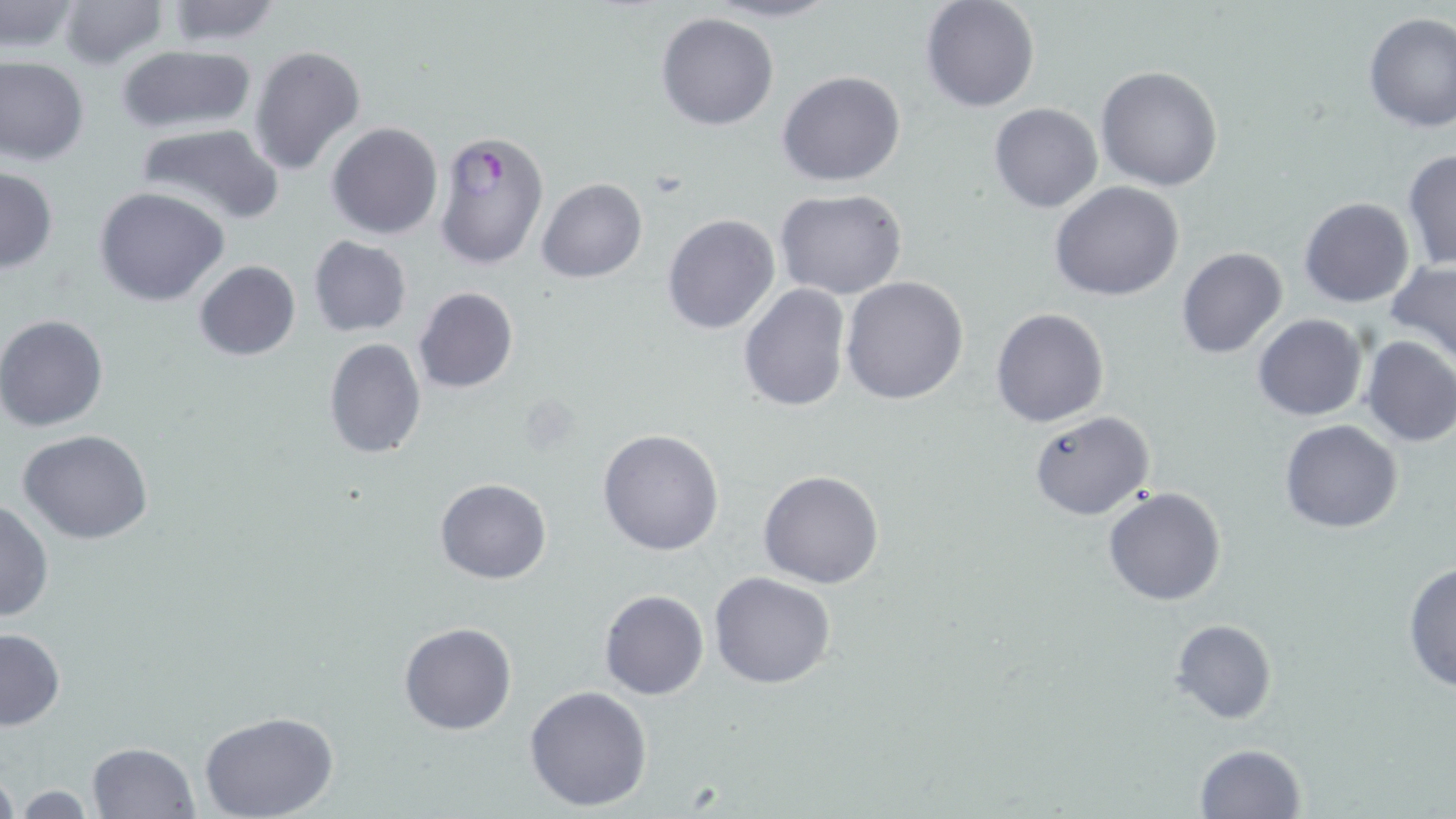
Summary:
  - Coordinate format: approximate bounding boxes as named x1/y1/x2/y2 corners in pixels
  - Uninfected red blood cell locations: (x1=58, y1=0, x2=167, y2=69), (x1=701, y1=0, x2=841, y2=24), (x1=919, y1=1, x2=1040, y2=113), (x1=1, y1=2, x2=80, y2=53), (x1=163, y1=2, x2=286, y2=48), (x1=655, y1=10, x2=780, y2=131), (x1=1361, y1=11, x2=1456, y2=131), (x1=114, y1=43, x2=260, y2=136), (x1=249, y1=44, x2=366, y2=178), (x1=0, y1=56, x2=89, y2=166), (x1=1095, y1=66, x2=1224, y2=191), (x1=777, y1=69, x2=907, y2=187), (x1=989, y1=103, x2=1104, y2=214), (x1=133, y1=122, x2=285, y2=227), (x1=327, y1=122, x2=444, y2=239), (x1=1401, y1=149, x2=1455, y2=272), (x1=0, y1=166, x2=58, y2=273), (x1=537, y1=178, x2=647, y2=283), (x1=1049, y1=181, x2=1184, y2=302), (x1=94, y1=186, x2=230, y2=306), (x1=774, y1=188, x2=908, y2=299), (x1=1299, y1=196, x2=1417, y2=308), (x1=661, y1=213, x2=780, y2=334), (x1=308, y1=236, x2=412, y2=336), (x1=1176, y1=248, x2=1288, y2=361), (x1=1386, y1=259, x2=1456, y2=366), (x1=193, y1=260, x2=301, y2=361), (x1=841, y1=277, x2=969, y2=405), (x1=738, y1=284, x2=851, y2=413), (x1=413, y1=287, x2=519, y2=395), (x1=990, y1=307, x2=1109, y2=428), (x1=0, y1=314, x2=108, y2=432), (x1=1252, y1=314, x2=1367, y2=421), (x1=1359, y1=336, x2=1456, y2=448), (x1=323, y1=337, x2=427, y2=460), (x1=1027, y1=410, x2=1155, y2=521), (x1=1278, y1=419, x2=1403, y2=534), (x1=597, y1=428, x2=725, y2=556), (x1=16, y1=429, x2=156, y2=546), (x1=759, y1=469, x2=886, y2=589), (x1=434, y1=478, x2=553, y2=585), (x1=1102, y1=487, x2=1226, y2=606), (x1=0, y1=498, x2=53, y2=625), (x1=1402, y1=560, x2=1456, y2=694), (x1=709, y1=572, x2=837, y2=691), (x1=599, y1=589, x2=709, y2=700), (x1=1170, y1=618, x2=1276, y2=725), (x1=399, y1=621, x2=517, y2=736), (x1=0, y1=628, x2=66, y2=732), (x1=524, y1=685, x2=655, y2=812), (x1=201, y1=712, x2=338, y2=819), (x1=86, y1=742, x2=200, y2=819), (x1=1194, y1=742, x2=1306, y2=818), (x1=0, y1=767, x2=20, y2=819), (x1=8, y1=784, x2=98, y2=816)
  - Plasmodium falciparum-infected red blood cell locations: (x1=431, y1=127, x2=550, y2=269)
  - Slide-level diagnosis: Plasmodium falciparum
  - Field of view: single
  - Magnification: 1000x
  - Stain: May-Grünwald-Giemsa
  - Preparation: thin blood smear
  - Image size: 1456×819 pixels
  - Modality: optical microscopy